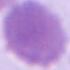
Summary:
  - Modality: photomicrograph
  - Magnification: 1000x
  - Identification: erythrocyte